Assess this cell for malaria.
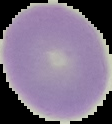

Uninfected.

Image is 112×124 pixels. From a thin blood film. Cell region segmented out of the field of view; the surrounding area is masked to black.